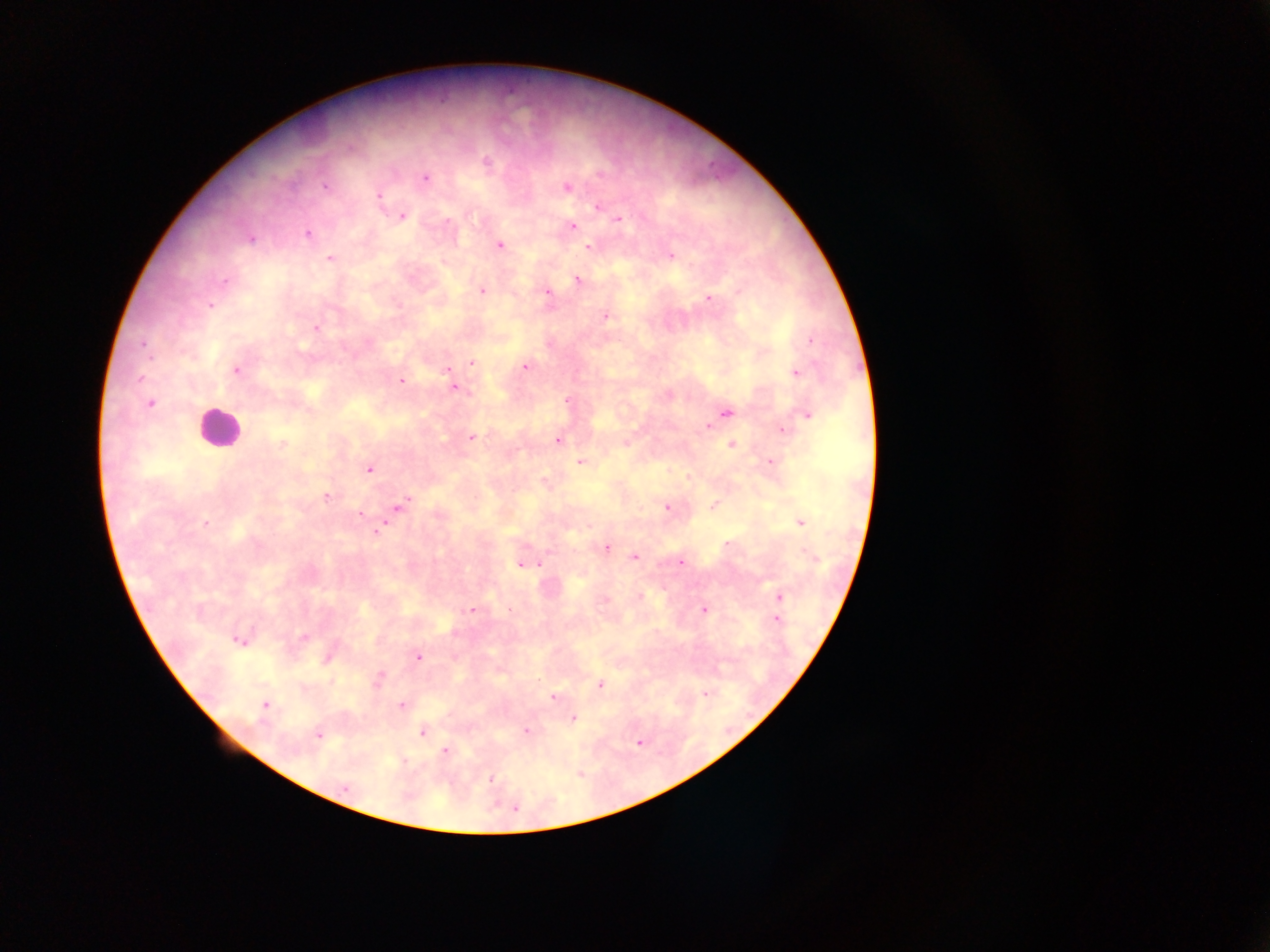

Approximate centers as {x, y} in pixels. Plasmodium parasite locations: {487, 161}, {601, 175}, {425, 178}, {326, 187}, {567, 188}, {379, 196}, {598, 206}, {402, 216}, {618, 219}, {574, 227}, {307, 234}, {252, 239}, {499, 245}, {588, 247}, {670, 256}, {330, 258}, {578, 280}, {224, 282}, {482, 291}, {546, 292}, {709, 299}, {211, 306}, {605, 317}, {317, 327}, {810, 341}, {142, 344}, {472, 363}, {525, 367}, {236, 370}, {447, 370}, {796, 372}, {139, 378}, {401, 381}, {455, 388}, {567, 400}, {149, 403}, {727, 413}, {807, 416}, {709, 427}, {783, 431}, {472, 437}, {558, 440}, {282, 445}, {732, 445}, {580, 461}, {771, 461}, {369, 469}, {326, 496}, {401, 505}, {714, 505}, {667, 507}, {359, 515}, {800, 522}, {205, 523}, {377, 531}, {727, 544}, {606, 548}, {635, 557}, {680, 563}, {539, 564}, {520, 565}, {639, 596}, {780, 596}, {472, 610}, {703, 610}, {776, 619}, {304, 637}, {238, 641}, {419, 657}, {327, 658}, {379, 677}, {600, 684}, {706, 694}, {553, 697}, {265, 705}, {402, 705}, {574, 719}, {525, 730}, {422, 732}, {319, 736}, {445, 751}, {491, 779}, {344, 788}, {515, 809}. Leukocyte locations: {218, 428}. One field of view. Photographed through a microscope with a mobile-phone camera. Thick blood smear. Collected in Ghana. Image is 1270×952 pixels.